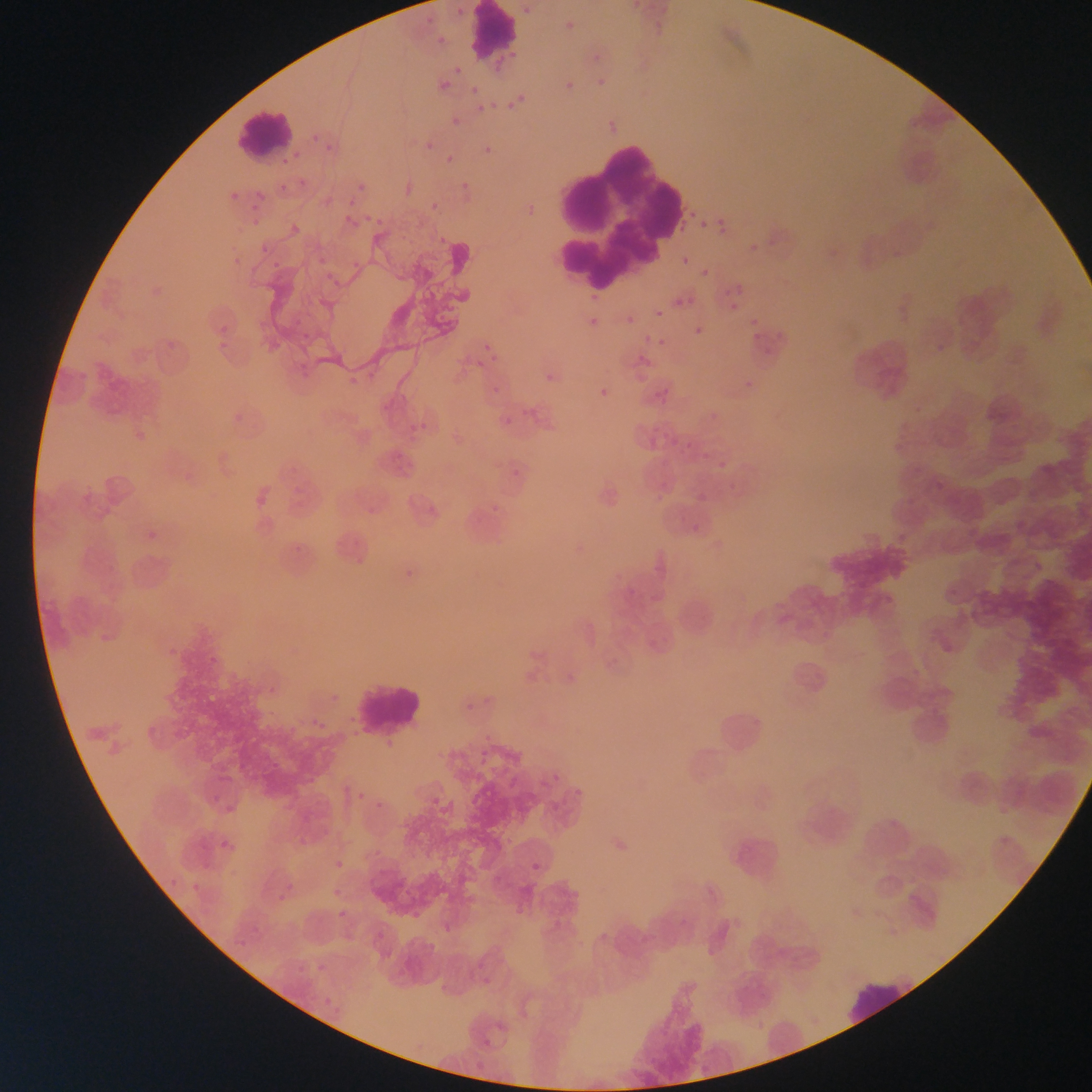

image size = 1092×1092 pixels
preparation = thin blood film
field of view = single
country = Ghana
objects each labeled both Plasmodium parasite and leukocyte by the source = approximate bounding boxes as [left, top, right, bottom] in pixels: [467, 3, 520, 64], [236, 105, 311, 170]
Plasmodium parasite locations = approximate bounding boxes as [left, top, right, bottom] in pixels: [452, 3, 467, 19], [519, 3, 535, 20], [562, 17, 579, 35], [433, 31, 450, 48], [588, 48, 607, 68], [450, 62, 466, 78], [437, 68, 461, 99], [593, 75, 611, 93], [434, 77, 454, 96], [561, 77, 579, 97], [466, 81, 483, 98], [504, 93, 529, 114], [474, 100, 491, 117], [447, 113, 464, 131], [309, 130, 324, 146], [322, 138, 339, 156], [422, 139, 437, 155], [479, 140, 497, 160], [443, 151, 457, 166], [457, 177, 474, 194], [353, 179, 369, 196], [340, 212, 359, 229], [714, 215, 733, 237], [697, 219, 709, 230], [436, 234, 450, 248], [745, 240, 763, 258], [679, 254, 691, 268], [268, 256, 285, 273], [699, 266, 712, 280], [727, 281, 749, 300], [670, 295, 688, 310], [725, 298, 741, 313], [663, 301, 686, 314], [653, 307, 666, 320], [582, 308, 604, 335], [622, 312, 638, 328], [746, 313, 763, 330], [691, 323, 708, 340], [748, 328, 766, 347], [654, 335, 669, 351], [479, 339, 499, 361], [474, 358, 487, 371], [541, 367, 562, 388], [593, 381, 617, 407], [491, 383, 505, 398], [521, 403, 540, 423], [499, 414, 514, 430], [412, 416, 433, 438], [354, 789, 367, 804], [527, 856, 547, 879]
capture = mobile-phone photograph through a microscope
leukocyte locations = approximate bounding boxes as [left, top, right, bottom] in pixels: [538, 122, 690, 299], [354, 677, 422, 735], [711, 697, 777, 763], [725, 823, 787, 889], [845, 974, 919, 1027]